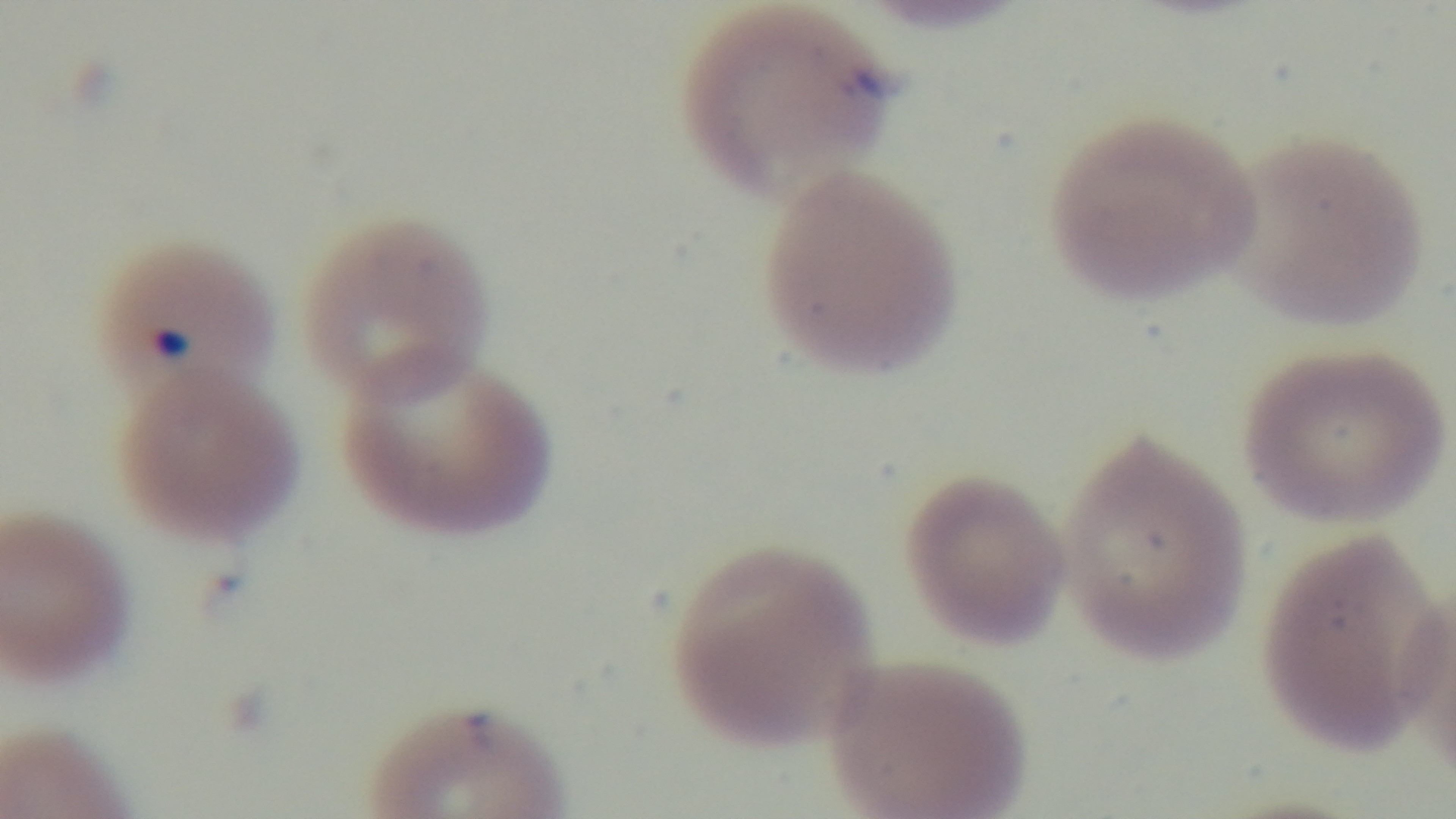

Preparation: thin blood film. Oil-immersion objective, 100x. Mounted 4K digital camera. Malaria status: infected. Single field of view. Giemsa-stained. Photomicrograph.